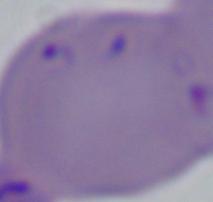
magnification = 1000x
modality = micrograph
identification = Babesia